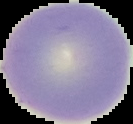
image_type: segmented cell region on a black background
image_size: 133×124 pixels
preparation: thin blood film
result: no malaria parasites detected